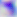 Micrograph. Toxoplasma gondii is shown. 400x magnification.